Outline each blood parasite and name the species.
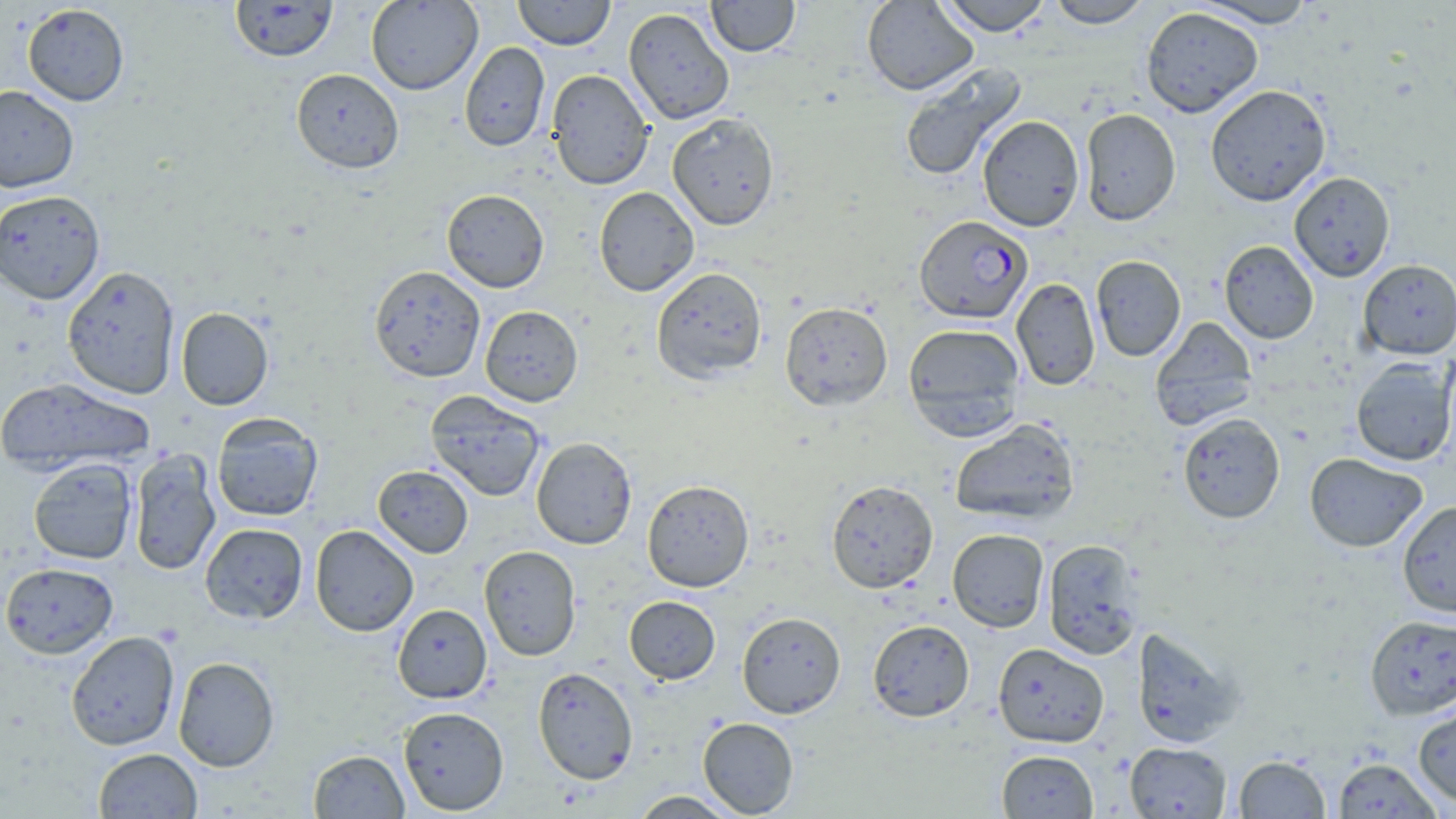
Approximate bounding boxes as named x1/y1/x2/y2 corners in pixels.
Plasmodium falciparum-infected red blood cells: (x1=914, y1=215, x2=1033, y2=324).
No Plasmodium ovale, Plasmodium malariae, Plasmodium vivax, Babesia divergens, or Trypanosoma brucei observed.

Summary:
  - Uninfected red blood cell locations: (x1=230, y1=0, x2=338, y2=62), (x1=365, y1=0, x2=483, y2=95), (x1=512, y1=0, x2=615, y2=49), (x1=706, y1=0, x2=800, y2=57), (x1=861, y1=0, x2=978, y2=95), (x1=936, y1=0, x2=1053, y2=35), (x1=1045, y1=0, x2=1154, y2=28), (x1=1193, y1=0, x2=1319, y2=28), (x1=22, y1=3, x2=129, y2=106), (x1=1140, y1=6, x2=1264, y2=118), (x1=623, y1=7, x2=734, y2=124), (x1=460, y1=41, x2=550, y2=151), (x1=898, y1=62, x2=1025, y2=183), (x1=291, y1=68, x2=404, y2=173), (x1=546, y1=69, x2=654, y2=190), (x1=1205, y1=84, x2=1331, y2=206), (x1=0, y1=85, x2=79, y2=193), (x1=1079, y1=108, x2=1181, y2=225), (x1=667, y1=113, x2=780, y2=230), (x1=977, y1=115, x2=1085, y2=232), (x1=1289, y1=171, x2=1395, y2=282), (x1=594, y1=187, x2=699, y2=296), (x1=0, y1=189, x2=106, y2=305), (x1=441, y1=189, x2=549, y2=293), (x1=1219, y1=240, x2=1319, y2=344), (x1=1090, y1=255, x2=1186, y2=361), (x1=1358, y1=259, x2=1456, y2=359), (x1=62, y1=265, x2=180, y2=399), (x1=369, y1=265, x2=486, y2=383), (x1=651, y1=267, x2=767, y2=383), (x1=1011, y1=277, x2=1100, y2=390), (x1=780, y1=301, x2=892, y2=410), (x1=480, y1=305, x2=583, y2=406), (x1=175, y1=307, x2=273, y2=410), (x1=1150, y1=317, x2=1258, y2=430), (x1=902, y1=323, x2=1026, y2=438), (x1=1350, y1=357, x2=1456, y2=466), (x1=0, y1=376, x2=154, y2=476), (x1=425, y1=390, x2=546, y2=502), (x1=211, y1=412, x2=323, y2=521), (x1=1178, y1=412, x2=1285, y2=523), (x1=949, y1=418, x2=1080, y2=525), (x1=531, y1=437, x2=637, y2=549), (x1=128, y1=449, x2=221, y2=576), (x1=1304, y1=452, x2=1428, y2=552), (x1=28, y1=457, x2=138, y2=564), (x1=373, y1=465, x2=473, y2=558), (x1=641, y1=479, x2=754, y2=592), (x1=826, y1=479, x2=938, y2=593), (x1=1397, y1=500, x2=1456, y2=617), (x1=199, y1=522, x2=309, y2=624), (x1=310, y1=524, x2=419, y2=636), (x1=947, y1=528, x2=1049, y2=631), (x1=1042, y1=539, x2=1144, y2=659), (x1=478, y1=545, x2=582, y2=661), (x1=1, y1=561, x2=119, y2=658), (x1=623, y1=596, x2=720, y2=684), (x1=392, y1=603, x2=492, y2=703), (x1=737, y1=611, x2=846, y2=718), (x1=1364, y1=614, x2=1456, y2=719), (x1=867, y1=619, x2=974, y2=721), (x1=1131, y1=626, x2=1243, y2=747), (x1=65, y1=631, x2=180, y2=751), (x1=993, y1=643, x2=1109, y2=748), (x1=172, y1=656, x2=279, y2=772), (x1=533, y1=667, x2=639, y2=784), (x1=1413, y1=705, x2=1456, y2=808), (x1=398, y1=706, x2=509, y2=815), (x1=698, y1=717, x2=799, y2=817), (x1=1124, y1=741, x2=1231, y2=818), (x1=93, y1=748, x2=202, y2=818), (x1=308, y1=749, x2=408, y2=818), (x1=996, y1=750, x2=1098, y2=818), (x1=1234, y1=754, x2=1330, y2=818), (x1=1332, y1=758, x2=1442, y2=818), (x1=629, y1=790, x2=742, y2=818)
  - Slide-level diagnosis: Plasmodium falciparum
  - Image size: 1456×819 pixels
  - Stain: May-Grünwald-Giemsa
  - Magnification: 1000x
  - Field of view: single
  - Preparation: thin blood smear
  - Modality: optical microscopy